Assess this cell for malaria.
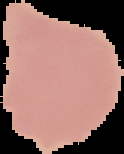

It is uninfected.

Segmented cell region on a black background. Image is 124×154 pixels. From a thin blood film.